Assess this cell for malaria.
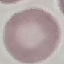
Uninfected.

stain: Giemsa
capture: smartphone camera at the microscope eyepiece
image_type: cell patch, automatically extracted from a larger field of view and resized to 64 × 64 pixels
preparation: thin blood smear